Assess this cell for malaria.
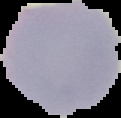
It is uninfected.

image type = cell region segmented out of the field of view; surrounding area masked to black
preparation = thin blood smear
image size = 121×118 pixels